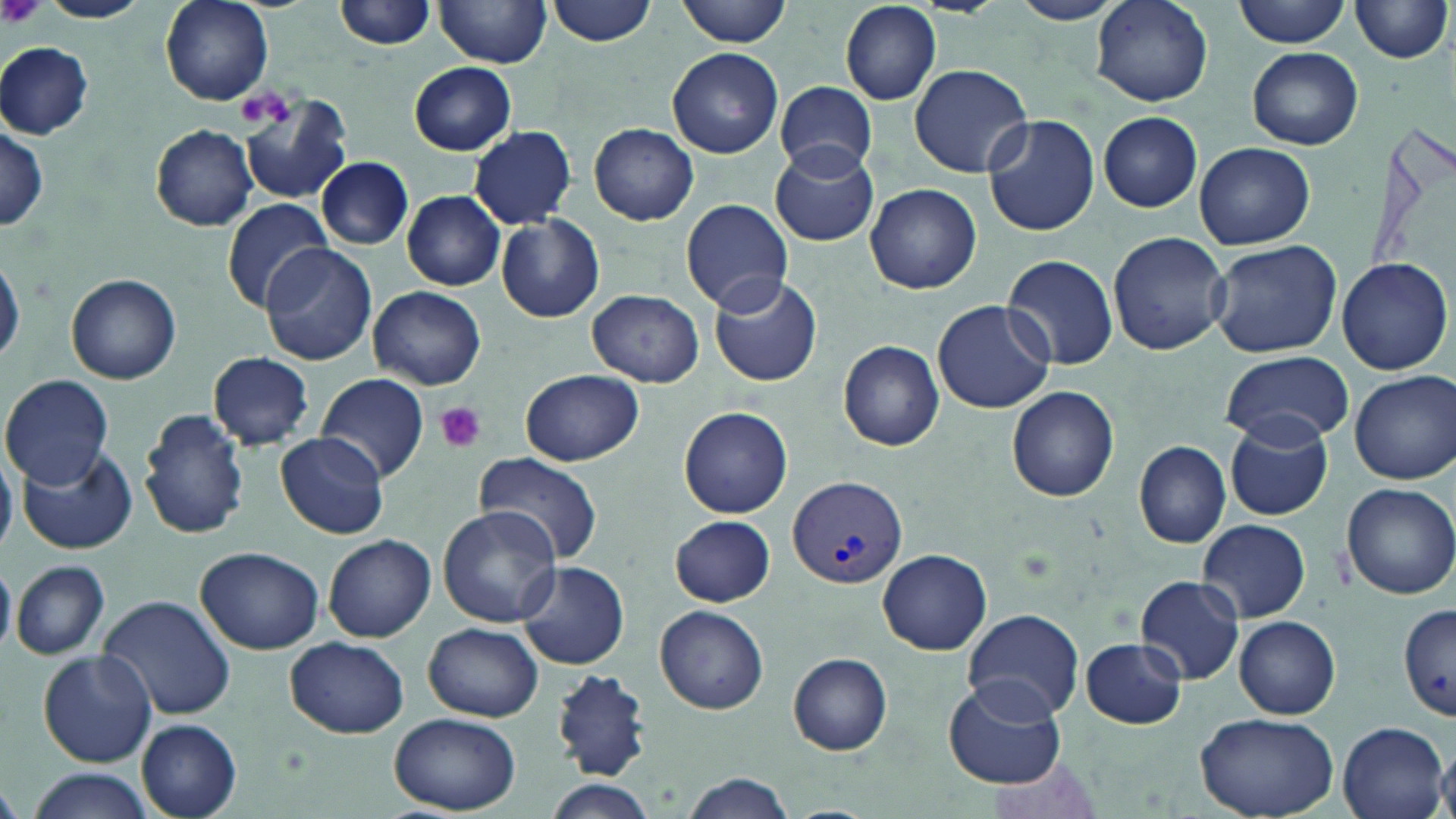
Summary:
  - Coordinate format: approximate bounding boxes as named x1/y1/x2/y2 corners in pixels
  - Platelet locations: (x1=2, y1=0, x2=45, y2=31), (x1=241, y1=85, x2=298, y2=131), (x1=433, y1=400, x2=488, y2=453)
  - Uninfected red blood cell locations: (x1=36, y1=0, x2=151, y2=23), (x1=158, y1=0, x2=273, y2=105), (x1=335, y1=0, x2=435, y2=51), (x1=547, y1=0, x2=658, y2=46), (x1=677, y1=0, x2=794, y2=46), (x1=1009, y1=0, x2=1125, y2=26), (x1=1235, y1=0, x2=1350, y2=48), (x1=1349, y1=0, x2=1451, y2=65), (x1=437, y1=1, x2=552, y2=68), (x1=841, y1=2, x2=941, y2=105), (x1=1092, y1=2, x2=1214, y2=107), (x1=1, y1=42, x2=94, y2=139), (x1=1246, y1=46, x2=1363, y2=149), (x1=667, y1=47, x2=784, y2=158), (x1=408, y1=62, x2=517, y2=155), (x1=909, y1=63, x2=1033, y2=178), (x1=774, y1=81, x2=877, y2=177), (x1=240, y1=97, x2=353, y2=207), (x1=1098, y1=111, x2=1203, y2=212), (x1=983, y1=114, x2=1100, y2=237), (x1=1, y1=124, x2=48, y2=233), (x1=151, y1=124, x2=258, y2=231), (x1=589, y1=124, x2=696, y2=225), (x1=468, y1=125, x2=577, y2=228), (x1=770, y1=142, x2=880, y2=248), (x1=1195, y1=142, x2=1315, y2=249), (x1=316, y1=156, x2=412, y2=249), (x1=864, y1=184, x2=981, y2=293), (x1=402, y1=190, x2=506, y2=290), (x1=222, y1=197, x2=332, y2=313), (x1=680, y1=197, x2=792, y2=313), (x1=495, y1=213, x2=605, y2=324), (x1=1108, y1=232, x2=1231, y2=356), (x1=1205, y1=240, x2=1344, y2=358), (x1=260, y1=242, x2=377, y2=367), (x1=0, y1=253, x2=23, y2=367), (x1=1001, y1=253, x2=1120, y2=371), (x1=1336, y1=255, x2=1452, y2=375), (x1=66, y1=273, x2=182, y2=385), (x1=708, y1=275, x2=823, y2=387), (x1=367, y1=285, x2=486, y2=391), (x1=587, y1=289, x2=703, y2=386), (x1=933, y1=300, x2=1056, y2=415), (x1=838, y1=340, x2=945, y2=451), (x1=1221, y1=350, x2=1353, y2=445), (x1=207, y1=351, x2=316, y2=451), (x1=519, y1=369, x2=645, y2=467), (x1=1351, y1=370, x2=1455, y2=484), (x1=1, y1=373, x2=115, y2=489), (x1=317, y1=374, x2=428, y2=485), (x1=1005, y1=386, x2=1119, y2=502), (x1=678, y1=405, x2=792, y2=518), (x1=137, y1=406, x2=250, y2=541), (x1=1224, y1=414, x2=1334, y2=522), (x1=275, y1=432, x2=390, y2=540), (x1=1134, y1=440, x2=1232, y2=548), (x1=17, y1=446, x2=138, y2=554), (x1=475, y1=451, x2=604, y2=566), (x1=1340, y1=482, x2=1455, y2=600), (x1=437, y1=507, x2=560, y2=629), (x1=671, y1=515, x2=775, y2=607), (x1=1197, y1=519, x2=1311, y2=622), (x1=322, y1=535, x2=436, y2=642), (x1=196, y1=547, x2=324, y2=656), (x1=879, y1=550, x2=990, y2=653), (x1=11, y1=559, x2=109, y2=661), (x1=517, y1=560, x2=630, y2=671), (x1=0, y1=562, x2=16, y2=656), (x1=1135, y1=575, x2=1245, y2=685), (x1=100, y1=595, x2=237, y2=720), (x1=1400, y1=602, x2=1456, y2=723), (x1=655, y1=605, x2=769, y2=713), (x1=962, y1=608, x2=1086, y2=721), (x1=1234, y1=616, x2=1341, y2=719), (x1=423, y1=623, x2=542, y2=722), (x1=286, y1=636, x2=409, y2=738), (x1=1080, y1=637, x2=1187, y2=729), (x1=38, y1=649, x2=157, y2=768), (x1=787, y1=653, x2=893, y2=755), (x1=546, y1=669, x2=652, y2=783), (x1=944, y1=676, x2=1066, y2=789), (x1=1192, y1=711, x2=1337, y2=819), (x1=389, y1=712, x2=523, y2=814), (x1=135, y1=718, x2=242, y2=819), (x1=1337, y1=719, x2=1449, y2=819), (x1=1435, y1=748, x2=1456, y2=818), (x1=20, y1=767, x2=157, y2=819), (x1=680, y1=773, x2=797, y2=819), (x1=539, y1=778, x2=657, y2=819)
  - Plasmodium vivax-infected red blood cell locations: (x1=787, y1=475, x2=907, y2=588)
  - Slide-level diagnosis: Plasmodium vivax
  - Field of view: one of a larger specimen
  - Preparation: thin blood smear
  - Magnification: 1000x
  - Modality: optical microscopy
  - Stain: May-Grünwald-Giemsa
  - Image size: 1456×819 pixels